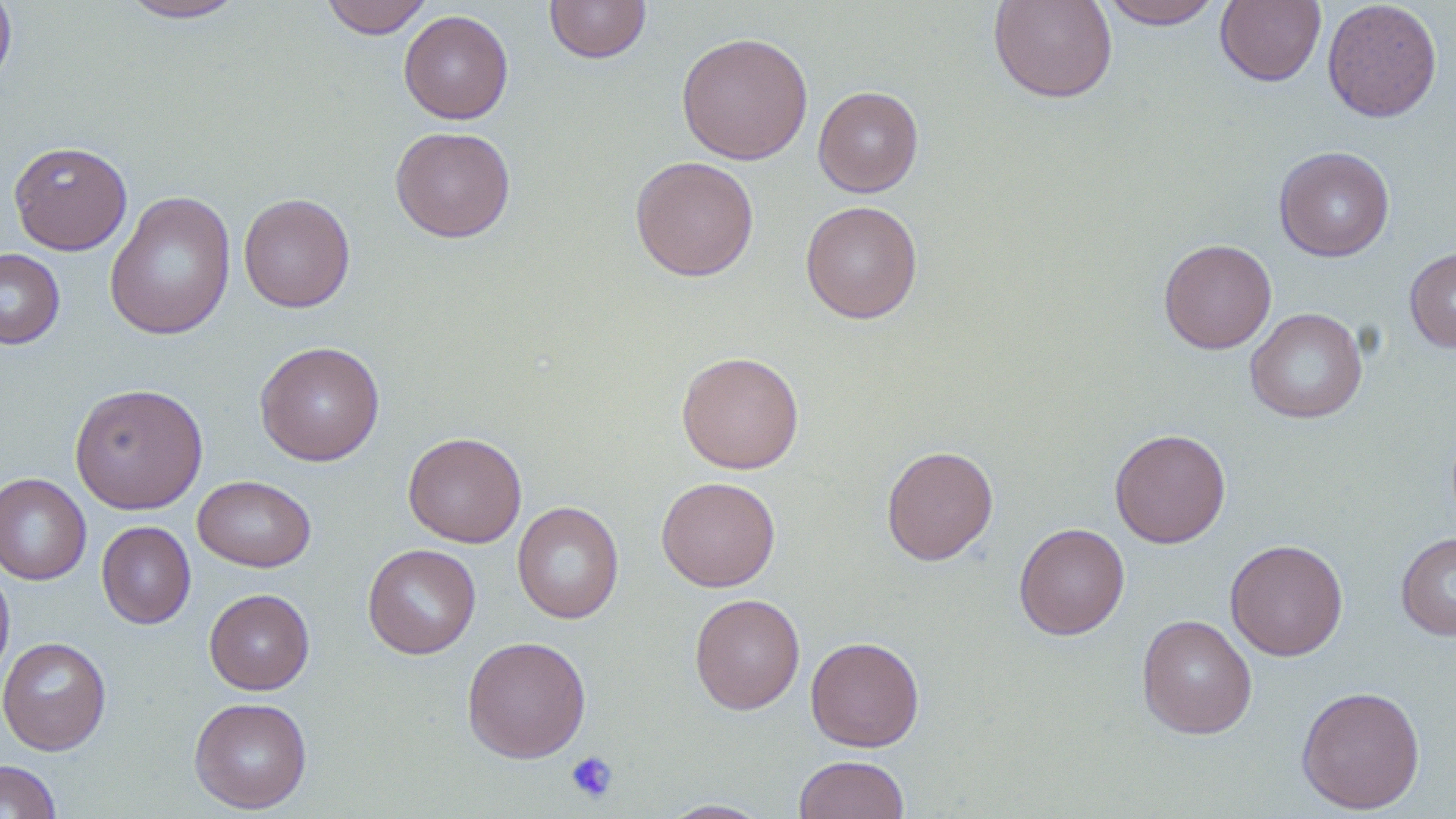
Approximate bounding boxes as [x1, y1, x2, y2] in pixels. Platelet locations: [565, 751, 619, 803]. Uninfected red blood cell locations: [0, 0, 17, 93], [320, 0, 434, 38], [544, 0, 652, 64], [988, 0, 1118, 104], [1099, 0, 1223, 29], [1215, 0, 1326, 87], [1322, 0, 1443, 122], [117, 1, 250, 22], [399, 10, 513, 124], [676, 31, 813, 165], [813, 85, 923, 197], [390, 126, 516, 242], [9, 140, 132, 255], [1274, 146, 1395, 261], [629, 156, 760, 281], [104, 190, 236, 341], [238, 193, 355, 313], [801, 200, 923, 323], [1158, 238, 1277, 354], [1405, 245, 1456, 354], [0, 248, 65, 349], [1245, 308, 1367, 423], [254, 340, 385, 466], [676, 350, 805, 474], [69, 383, 208, 513], [1109, 428, 1231, 548], [402, 431, 526, 548], [881, 445, 998, 565], [0, 473, 91, 585], [192, 475, 316, 572], [656, 475, 781, 592], [512, 501, 624, 624], [96, 521, 196, 628], [1014, 522, 1130, 639], [1396, 532, 1456, 640], [1225, 539, 1348, 661], [362, 543, 481, 659], [0, 562, 15, 689], [204, 588, 315, 695], [689, 593, 805, 715], [1136, 613, 1258, 739], [805, 635, 924, 752], [0, 636, 111, 755], [461, 636, 591, 763], [1295, 685, 1426, 814], [188, 696, 313, 814], [795, 755, 910, 819], [0, 760, 62, 819], [659, 799, 773, 818]. Slide-level diagnosis: no evidence of blood parasites. Single field of view. Captured at 1000x magnification. Light microscopy. Image is 1456×819 pixels. Thin blood smear. May-Grünwald-Giemsa-stained preparation.